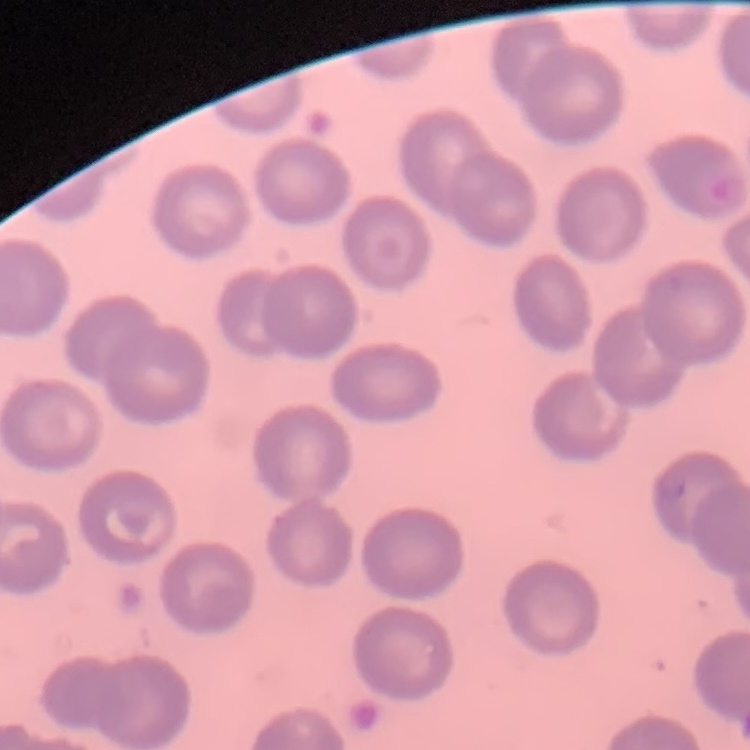
Summary:
  - Red blood cell morphology: no rouleaux formation
  - Preparation: thin blood film
  - Stain: Field's or Giemsa
  - Image type: one tile cut from a larger photomicrograph